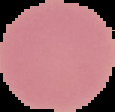

Cell region segmented out of the field of view; the surrounding area is masked to black. From a thin blood smear. Malaria status: uninfected. Image is 115×112 pixels.